Locate every malaria parasite.
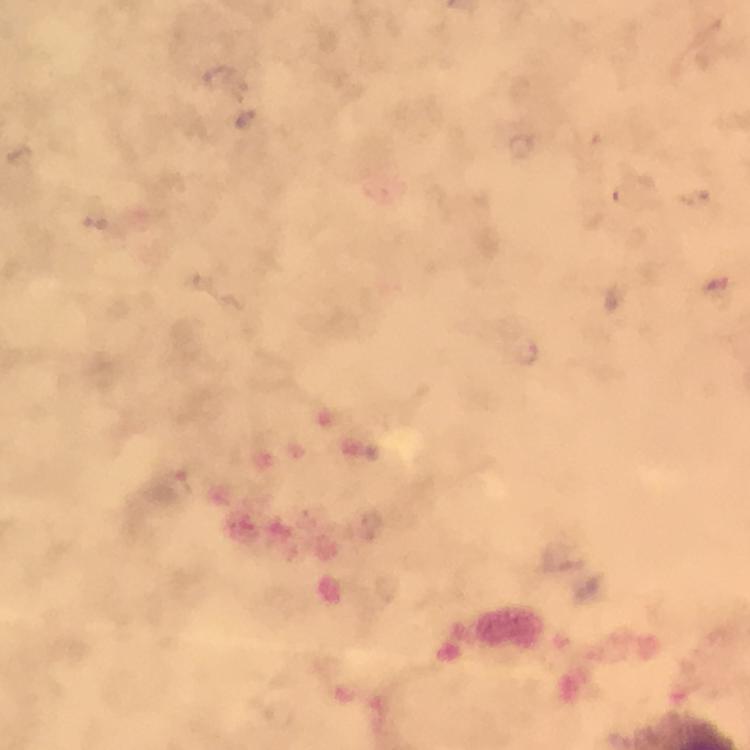

Approximate centers as {x, y} in pixels.
Malaria parasites: {219, 77}, {247, 118}, {523, 147}, {529, 350}.

Summary:
  - Preparation: thick smear
  - Context: from a malaria diagnostic workup
  - Image size: 750×750 pixels
  - Stain: Giemsa
  - Cropped from: one field of view
  - Magnification: 100x
  - Capture: smartphone camera through the microscope
  - Immersion oil: applied